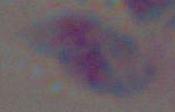
magnification: 1000x
modality: micrograph
identification: Toxoplasma gondii